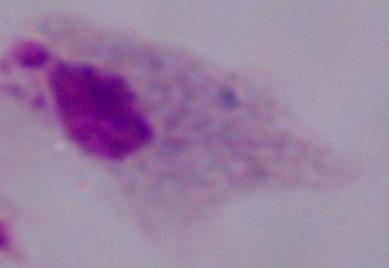
A trichomonad is seen. 1000x magnification. Photomicrograph.